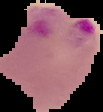

image type = segmented cell region with the area outside set to black
preparation = thin blood smear
image size = 103×112 pixels
result = Plasmodium parasites identified